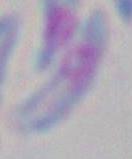
Summary:
  - Modality: micrograph
  - Identification: Toxoplasma gondii
  - Magnification: 1000x